Locate every uninfected red blood cell.
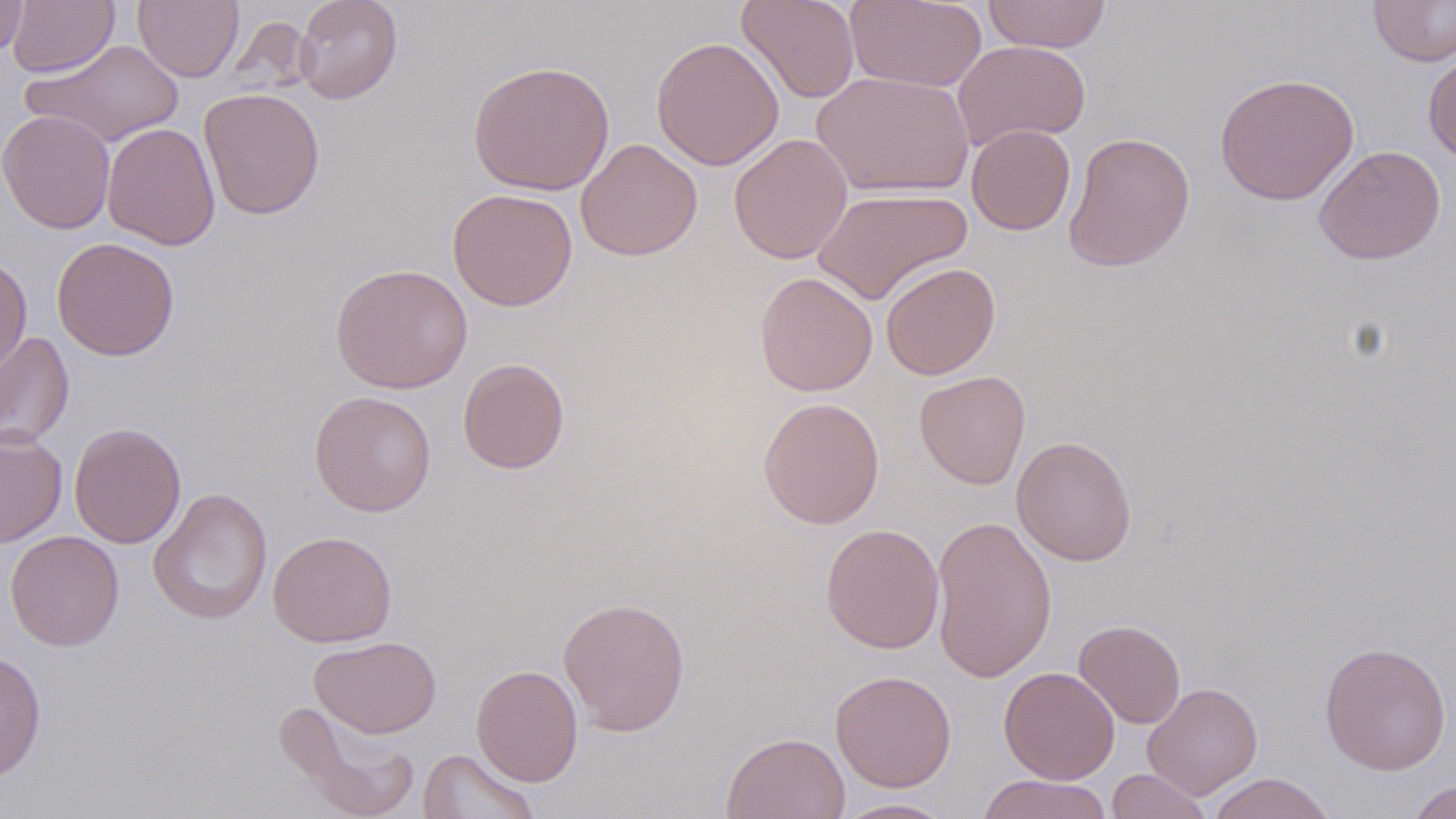

Approximate bounding boxes as [x1, y1, x2, y2] in pixels.
Uninfected red blood cells: [7, 0, 119, 77], [133, 0, 244, 82], [294, 0, 403, 104], [737, 0, 860, 104], [846, 0, 987, 91], [981, 0, 1112, 53], [1368, 0, 1456, 66], [0, 1, 29, 59], [651, 36, 784, 171], [22, 38, 185, 148], [952, 38, 1091, 150], [1423, 50, 1456, 163], [468, 60, 615, 196], [812, 70, 975, 199], [1214, 73, 1359, 206], [199, 87, 325, 220], [1, 110, 116, 234], [102, 122, 221, 250], [966, 124, 1076, 235], [1063, 131, 1196, 273], [728, 133, 853, 264], [576, 138, 703, 261], [1314, 144, 1446, 265], [813, 187, 972, 305], [447, 188, 578, 311], [52, 237, 180, 361], [0, 254, 33, 379], [881, 262, 1001, 380], [330, 263, 473, 393], [754, 272, 878, 397], [0, 330, 75, 451], [457, 358, 570, 474], [914, 370, 1030, 489], [309, 390, 436, 517], [757, 397, 885, 529], [69, 422, 186, 549], [0, 428, 67, 548], [1011, 435, 1137, 566], [148, 487, 273, 625], [930, 514, 1058, 682], [821, 523, 945, 654], [5, 530, 124, 651], [267, 530, 397, 647], [558, 596, 691, 736], [1073, 619, 1186, 729], [309, 635, 442, 739], [1319, 641, 1452, 775], [0, 649, 47, 782], [470, 664, 584, 787], [998, 666, 1120, 784], [830, 669, 957, 792], [1142, 681, 1263, 799], [273, 699, 420, 819], [721, 731, 851, 819], [418, 747, 541, 819], [1107, 768, 1213, 819], [1205, 772, 1337, 819], [976, 773, 1113, 819], [1404, 778, 1456, 819], [832, 798, 958, 818].

Summary:
  - Slide-level diagnosis: no evidence of blood parasites
  - Image size: 1456×819 pixels
  - Field of view: single
  - Stain: May-Grünwald-Giemsa
  - Preparation: thin blood smear
  - Magnification: 1000x
  - Modality: light microscopy